Identify the cell.
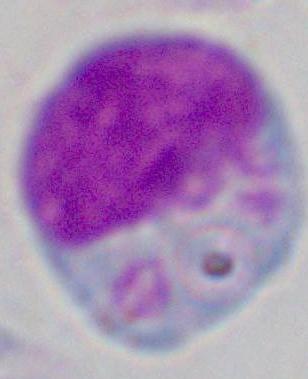

This is a leukocyte.

Summary:
  - Magnification: 1000x
  - Modality: micrograph